Give the position of every Plasmodium parasite and every leukocyte.
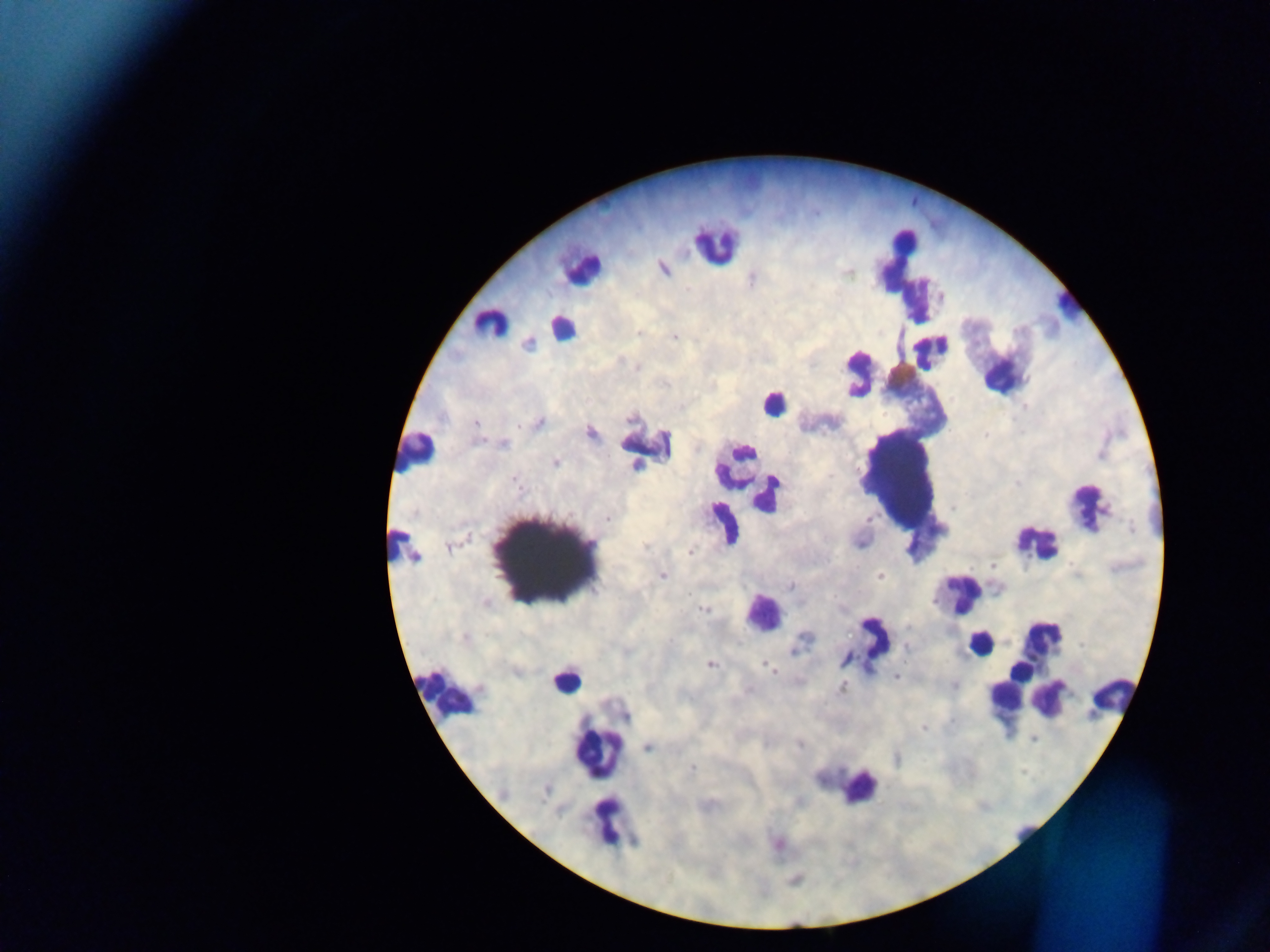
Approximate centers as (x, y) in pixels.
Plasmodium parasites: (663, 268), (848, 272), (489, 323), (639, 333), (675, 337), (528, 344), (638, 367), (681, 405), (539, 422), (476, 423), (591, 432), (505, 444), (555, 462), (516, 483), (608, 518), (870, 520), (1132, 528), (860, 543), (644, 547), (449, 548), (690, 552), (415, 558), (992, 565), (662, 575), (880, 575), (791, 586), (934, 601), (486, 602), (704, 609), (464, 637), (805, 637), (906, 647), (793, 651), (845, 660), (711, 664), (769, 667), (896, 676), (954, 685), (842, 688), (626, 716), (923, 728), (1033, 740), (800, 745), (648, 747), (897, 759), (692, 769).
Leukocytes (some below the resolvable threshold): (715, 243), (582, 268), (903, 270), (1066, 305), (560, 327), (933, 351), (997, 352), (856, 372), (774, 403), (644, 445), (416, 452), (734, 465), (899, 479), (775, 483), (763, 504), (1086, 507), (723, 523), (1034, 541), (396, 543), (549, 557), (962, 592), (762, 613), (876, 638), (978, 643), (1041, 644), (565, 679), (1041, 679), (447, 693), (1116, 695), (1002, 698), (1050, 699), (599, 752), (858, 787), (606, 820).

Mobile-phone photograph taken through the microscope. Image is 1270×952 pixels. One field of view. Sample from Ghana. Thick blood smear.